Assess the morphology of the erythrocytes.
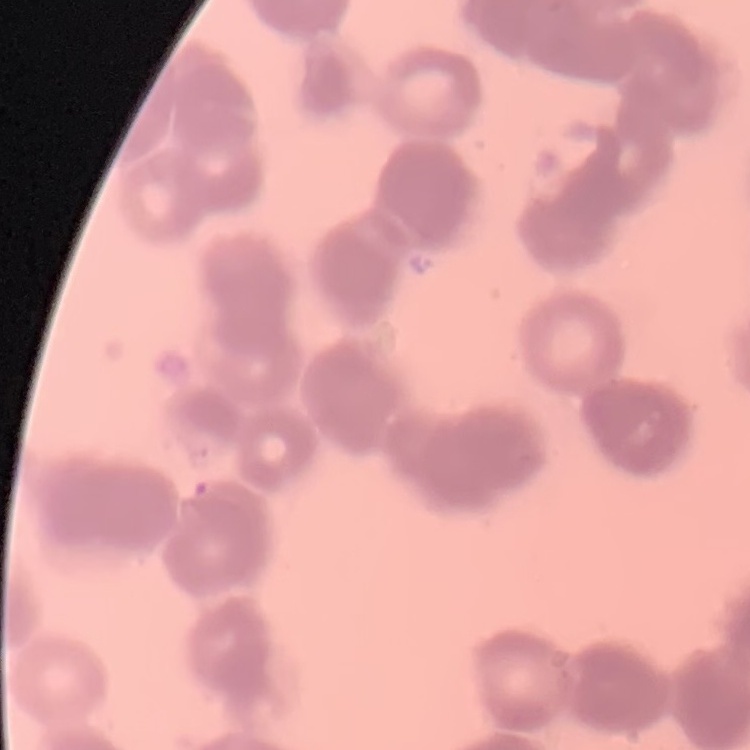
They show rouleaux formation.

preparation: thin peripheral smear
stain: Field's or Giemsa
image_type: one tile cut from a larger photomicrograph